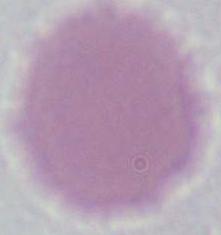
Summary:
  - Modality: photomicrograph
  - Identification: erythrocyte
  - Magnification: 1000x